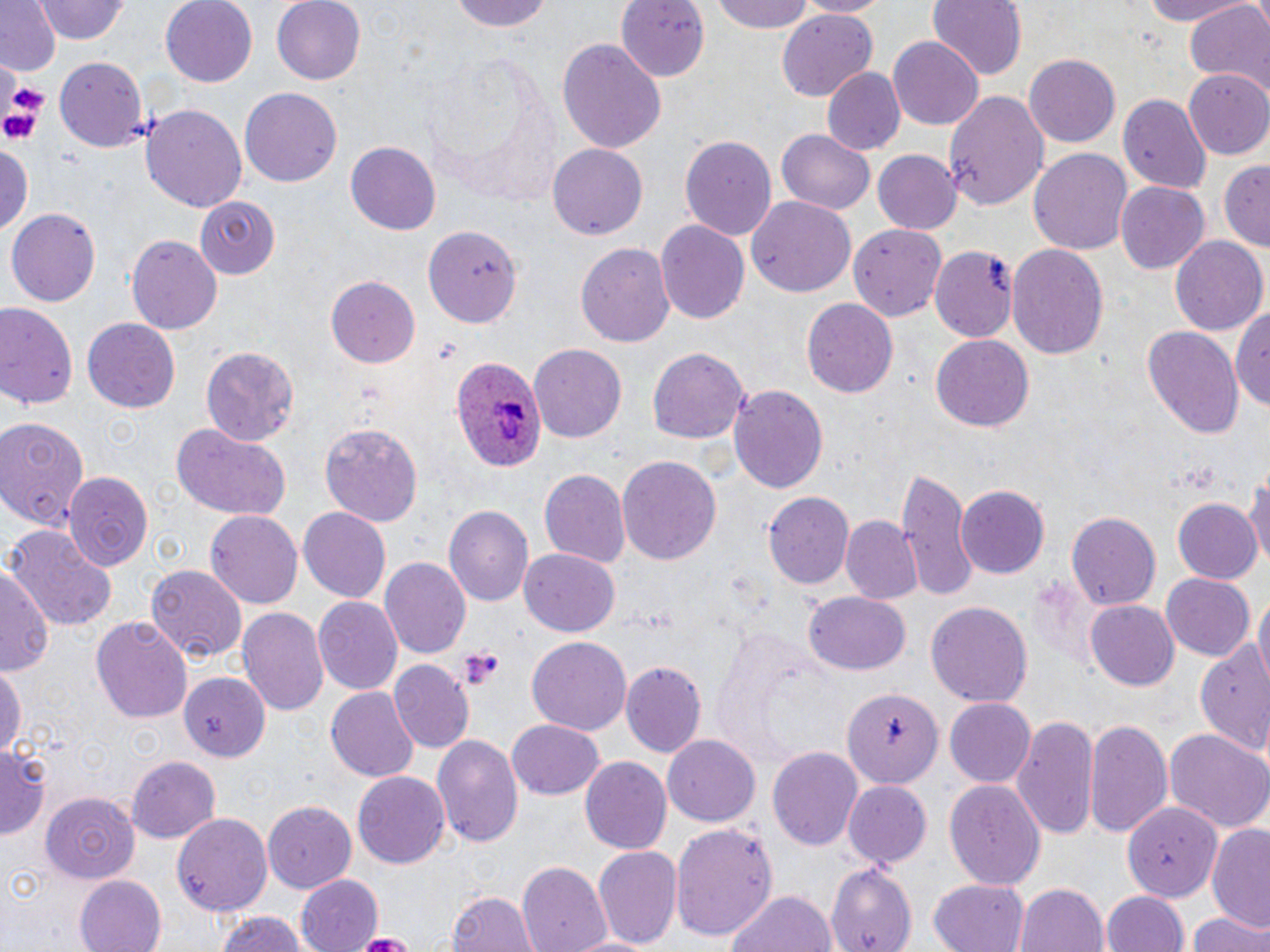
slide_level_diagnosis: Plasmodium ovale
field_of_view: one of a larger specimen
plasmodium_ovale_infected_red_blood_cell_locations: 'approximate bounding boxes as [x1, y1, x2, y2] in pixels: [452, 354, 543, 474]'
magnification: 1000x
preparation: thin blood smear
modality: optical microscopy
platelet_locations: 'approximate bounding boxes as [x1, y1, x2, y2] in pixels: [0, 91, 46, 145], [459, 646, 506, 689]'
image_size: 1270×952 pixels
stain: May-Grünwald-Giemsa
uninfected_red_blood_cell_locations: 'approximate bounding boxes as [x1, y1, x2, y2] in pixels: [0, 0, 60, 75], [35, 0, 129, 44], [161, 0, 259, 87], [272, 0, 366, 86], [452, 0, 555, 33], [616, 0, 708, 81], [708, 0, 819, 34], [796, 0, 893, 17], [927, 0, 1026, 81], [1133, 0, 1253, 25], [1185, 1, 1270, 95], [776, 9, 879, 101], [889, 36, 986, 130], [557, 38, 666, 152], [1026, 54, 1121, 147], [55, 57, 148, 150], [822, 68, 905, 155], [1184, 69, 1270, 159], [241, 87, 342, 190], [945, 89, 1049, 212], [1118, 98, 1210, 194], [141, 103, 246, 213], [776, 129, 876, 214], [678, 133, 778, 241], [548, 141, 646, 237], [0, 142, 32, 237], [345, 142, 441, 235], [1027, 147, 1133, 257], [871, 149, 959, 235], [1219, 158, 1268, 253], [1116, 181, 1209, 273], [192, 195, 282, 277], [747, 197, 856, 299], [7, 208, 101, 306], [656, 219, 749, 323], [849, 225, 945, 323], [425, 226, 520, 328], [126, 235, 224, 334], [1171, 237, 1267, 336], [578, 240, 675, 350], [1007, 243, 1108, 358], [930, 244, 1021, 346], [326, 273, 421, 368], [802, 298, 898, 399], [0, 303, 79, 411], [1232, 303, 1270, 411], [81, 318, 181, 414], [1142, 326, 1245, 442], [930, 334, 1035, 432], [201, 343, 302, 444], [529, 343, 627, 445], [647, 347, 750, 444], [729, 383, 829, 492], [0, 414, 88, 529], [169, 422, 292, 522], [321, 423, 424, 525], [616, 456, 722, 565], [1243, 460, 1270, 579], [539, 468, 629, 569], [898, 469, 973, 604], [62, 472, 153, 568], [957, 484, 1048, 577], [763, 492, 854, 589], [1172, 499, 1260, 583], [297, 506, 389, 600], [444, 506, 531, 605], [205, 510, 303, 610], [1066, 511, 1160, 611], [840, 517, 922, 605], [4, 525, 116, 634], [519, 548, 620, 636], [380, 556, 470, 656], [1, 564, 56, 678], [147, 565, 246, 666], [1161, 573, 1255, 661], [802, 592, 911, 677], [1252, 592, 1270, 687], [313, 597, 402, 696], [1086, 600, 1180, 691], [925, 602, 1033, 709], [236, 607, 329, 717], [92, 617, 192, 722], [525, 636, 632, 735], [1194, 636, 1270, 757], [390, 659, 472, 751], [0, 660, 25, 763], [621, 661, 706, 757], [181, 670, 269, 761], [326, 688, 418, 782], [844, 688, 944, 790], [944, 698, 1037, 788], [1011, 715, 1101, 835], [1085, 717, 1174, 836], [507, 719, 605, 800], [1163, 726, 1270, 830], [432, 734, 524, 851], [662, 735, 760, 825], [0, 743, 48, 842], [768, 746, 863, 850], [125, 757, 220, 841], [580, 757, 672, 856], [353, 771, 452, 868], [944, 780, 1046, 891], [843, 782, 932, 866], [41, 792, 138, 883], [1123, 800, 1220, 904], [262, 801, 355, 894], [172, 811, 272, 916], [670, 822, 777, 939], [1205, 823, 1270, 928], [594, 844, 683, 947], [517, 861, 612, 952], [826, 863, 917, 952], [74, 873, 165, 952], [294, 874, 384, 952], [928, 878, 1031, 952], [1014, 882, 1109, 952], [723, 886, 838, 952], [447, 889, 538, 952], [1102, 890, 1190, 952], [1185, 909, 1270, 952], [211, 910, 314, 952], [353, 931, 415, 950], [567, 933, 658, 951]'